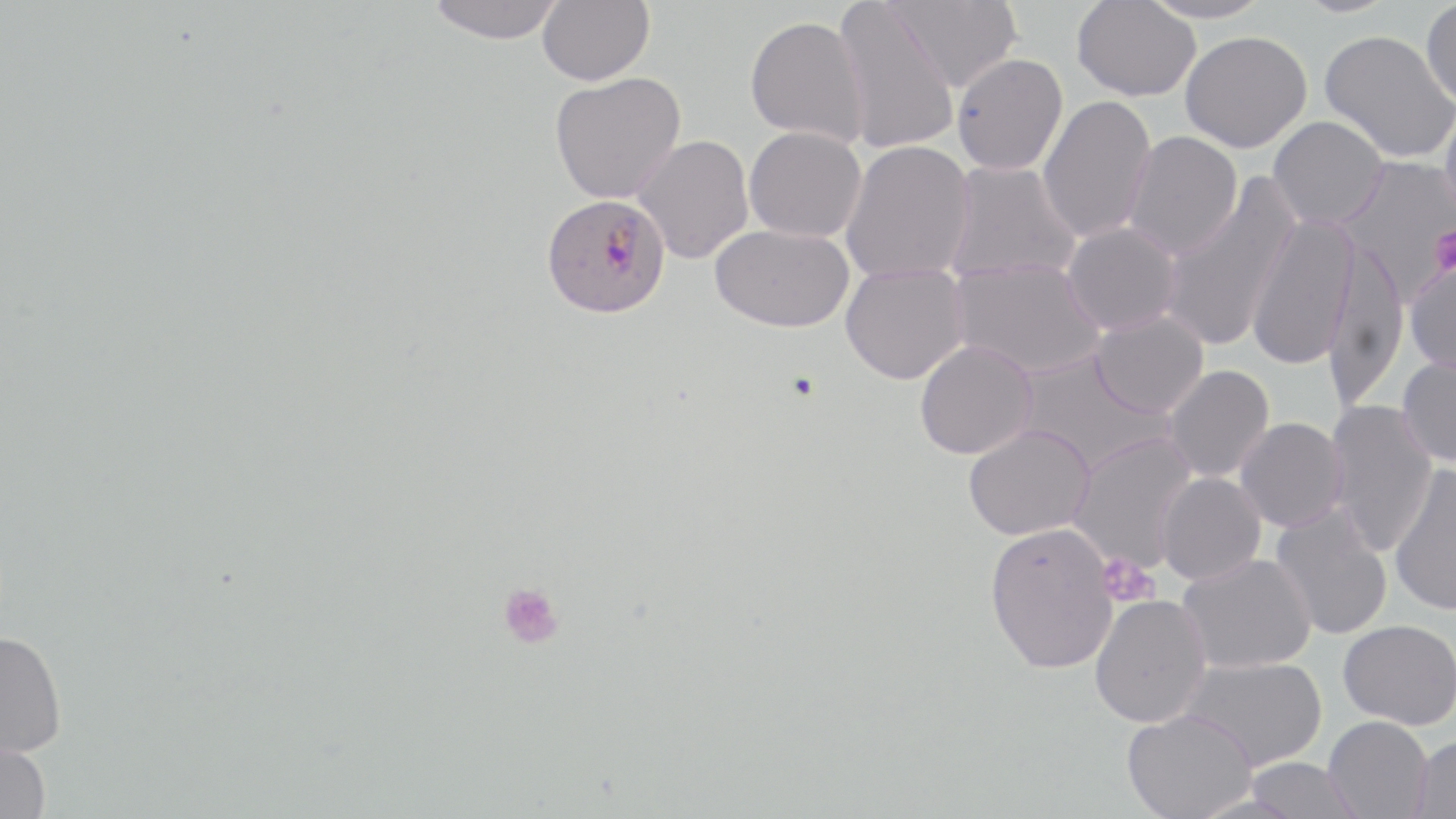
Summary:
  - Coordinate format: approximate bounding boxes as (x1, y1, x2, y2) in pixels
  - Plasmodium falciparum-infected red blood cell locations: (541, 193, 671, 319)
  - Platelet locations: (1429, 225, 1456, 275), (1097, 553, 1158, 607), (498, 582, 564, 649)
  - Uninfected red blood cell locations: (427, 0, 565, 44), (833, 0, 960, 155), (885, 0, 1022, 92), (1136, 0, 1274, 24), (1292, 0, 1400, 17), (537, 1, 654, 86), (1072, 1, 1201, 102), (1421, 1, 1456, 109), (745, 13, 870, 147), (1319, 29, 1456, 164), (1180, 31, 1312, 152), (952, 53, 1068, 175), (549, 71, 686, 204), (1037, 94, 1156, 244), (1439, 99, 1456, 226), (1268, 116, 1388, 230), (744, 126, 866, 242), (1122, 131, 1243, 260), (633, 135, 753, 264), (841, 140, 976, 283), (1334, 155, 1456, 303), (942, 162, 1082, 285), (1158, 179, 1300, 353), (1246, 215, 1359, 370), (1062, 221, 1182, 335), (710, 224, 854, 333), (1322, 239, 1408, 409), (950, 258, 1106, 379), (1405, 259, 1456, 377), (839, 262, 970, 385), (1089, 312, 1208, 418), (914, 340, 1037, 459), (1014, 351, 1175, 477), (1397, 353, 1456, 467), (1162, 364, 1274, 483), (1324, 400, 1438, 557), (1235, 417, 1348, 533), (962, 424, 1095, 540), (1067, 432, 1198, 573), (1389, 462, 1456, 616), (1155, 472, 1266, 586), (1270, 504, 1392, 641), (984, 522, 1119, 674), (1177, 553, 1316, 673), (1089, 595, 1211, 727), (1338, 619, 1456, 729), (0, 631, 67, 758), (1180, 656, 1328, 771), (1121, 709, 1258, 819), (1324, 716, 1433, 819), (1409, 734, 1456, 819), (0, 737, 51, 819), (1243, 757, 1363, 819)
  - Slide-level diagnosis: Plasmodium falciparum
  - Stain: May-Grünwald-Giemsa
  - Image size: 1456×819 pixels
  - Modality: optical microscopy
  - Field of view: one of a larger specimen
  - Magnification: 1000x
  - Preparation: thin blood film